Point out each malaria parasite and each leukocyte.
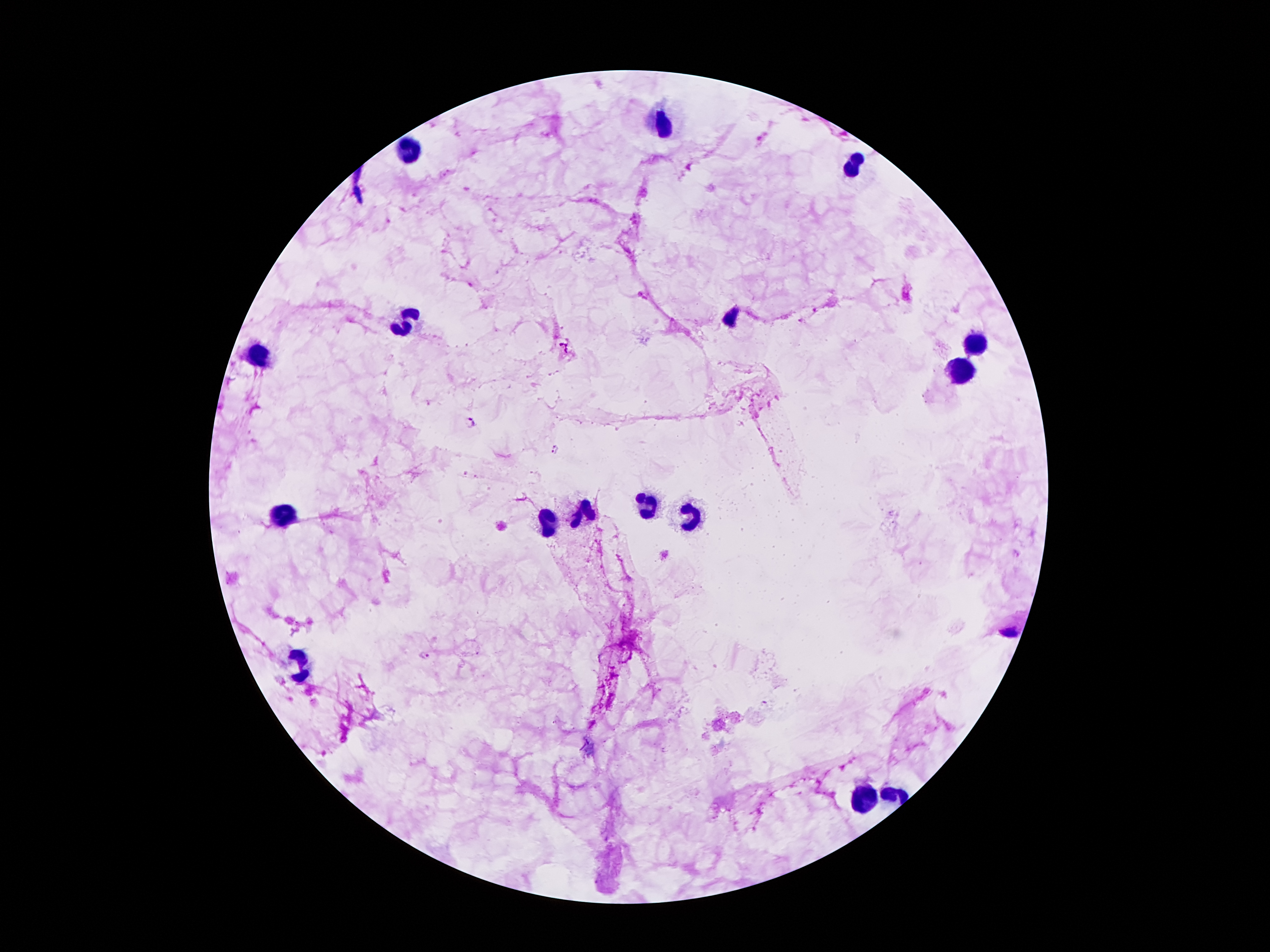

Approximate object centers, in pixels from the top-left corner.
Malaria parasites: (x=816, y=310), (x=801, y=321), (x=563, y=347), (x=471, y=423), (x=555, y=449), (x=425, y=655).
Leukocytes: (x=665, y=126), (x=409, y=149), (x=856, y=163), (x=409, y=323), (x=973, y=341), (x=259, y=350), (x=959, y=371), (x=645, y=509), (x=581, y=510), (x=283, y=513), (x=687, y=517), (x=546, y=524), (x=303, y=664), (x=893, y=794), (x=869, y=798).

Photographed through the microscope eyepiece with a smartphone camera. Giemsa-stained preparation. Thick blood film. Image is 1270×952 pixels. Single field of view. 100x magnification. Patient malaria status: infected with Plasmodium falciparum.